Name the parasite shown.
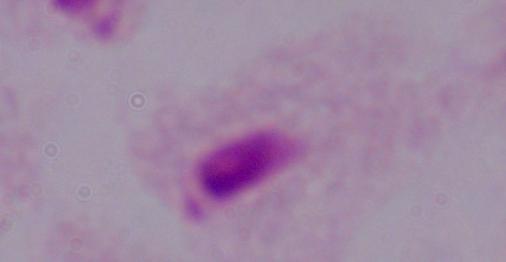

This is a trichomonad.

Photomicrograph. 1000x magnification.